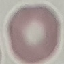
Summary:
  - Result: negative for malaria parasites
  - Image type: automatically extracted cell patch, resized to 64 × 64 pixels
  - Preparation: thin smear
  - Capture: smartphone camera at the microscope eyepiece
  - Stain: Giemsa